Classify this cell by malaria status.
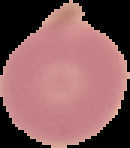
Uninfected.

{
  "image_type": "cell region segmented out of the field of view; surrounding area masked to black",
  "preparation": "thin blood smear",
  "image_size": "130×148 pixels"
}